Assess the morphology of the red blood cells.
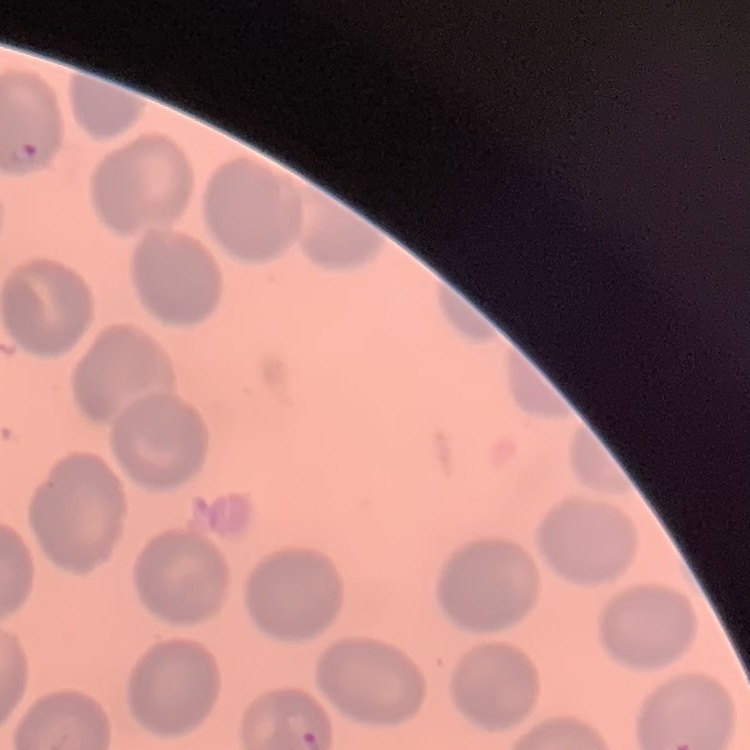
No rouleaux formation.

{
  "image_type": "square crop of a larger photomicrograph",
  "stain": "Field's or Giemsa",
  "preparation": "thin blood film"
}